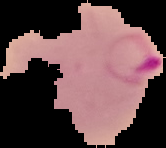

Malaria status: parasitized. From a thin blood film. Image is 166×148 pixels. Cell region segmented out of the field of view; the surrounding area is masked to black.